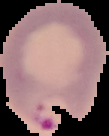

image_size: 109×136 pixels
image_type: cell region segmented out of the field of view; surrounding area masked to black
result: Plasmodium parasites detected
preparation: thin blood film